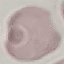

Summary:
  - Result: negative for malaria parasites
  - Stain: Giemsa
  - Image type: automatically extracted cell patch, resized to 64 × 64 pixels
  - Capture: smartphone through the microscope eyepiece
  - Preparation: thin blood film